Name the cell type shown.
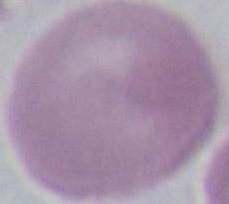

This is an erythrocyte.

1000x magnification. Photomicrograph.